Assess the morphology of the erythrocytes.
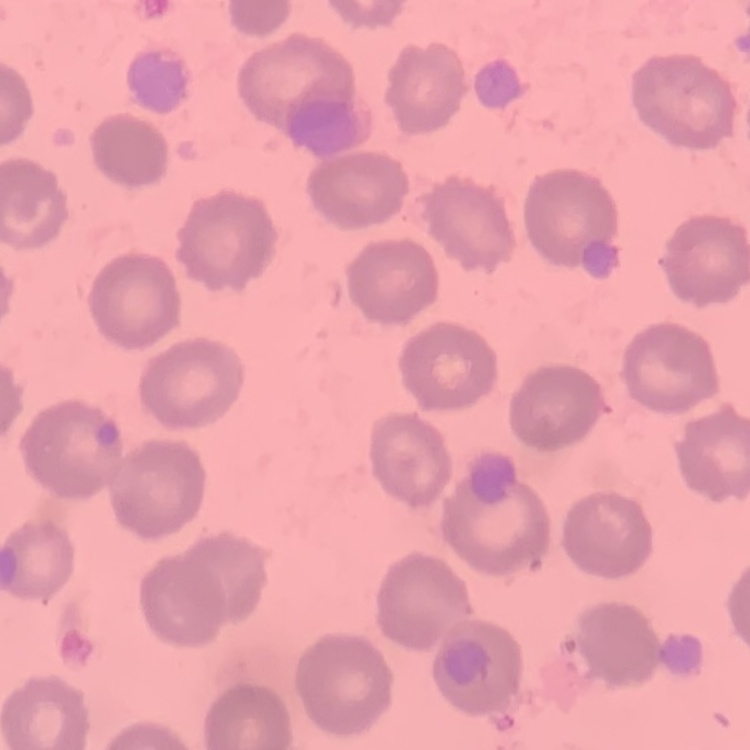

They show no rouleaux formation.

Thin blood smear. Stained with either Field's or Giemsa. Square crop of a larger photomicrograph.